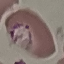
malaria status = parasitized
preparation = thin smear
image type = cell patch, automatically extracted from a larger field of view and resized to 64 × 64 pixels
stain = Giemsa
capture = smartphone through the microscope eyepiece